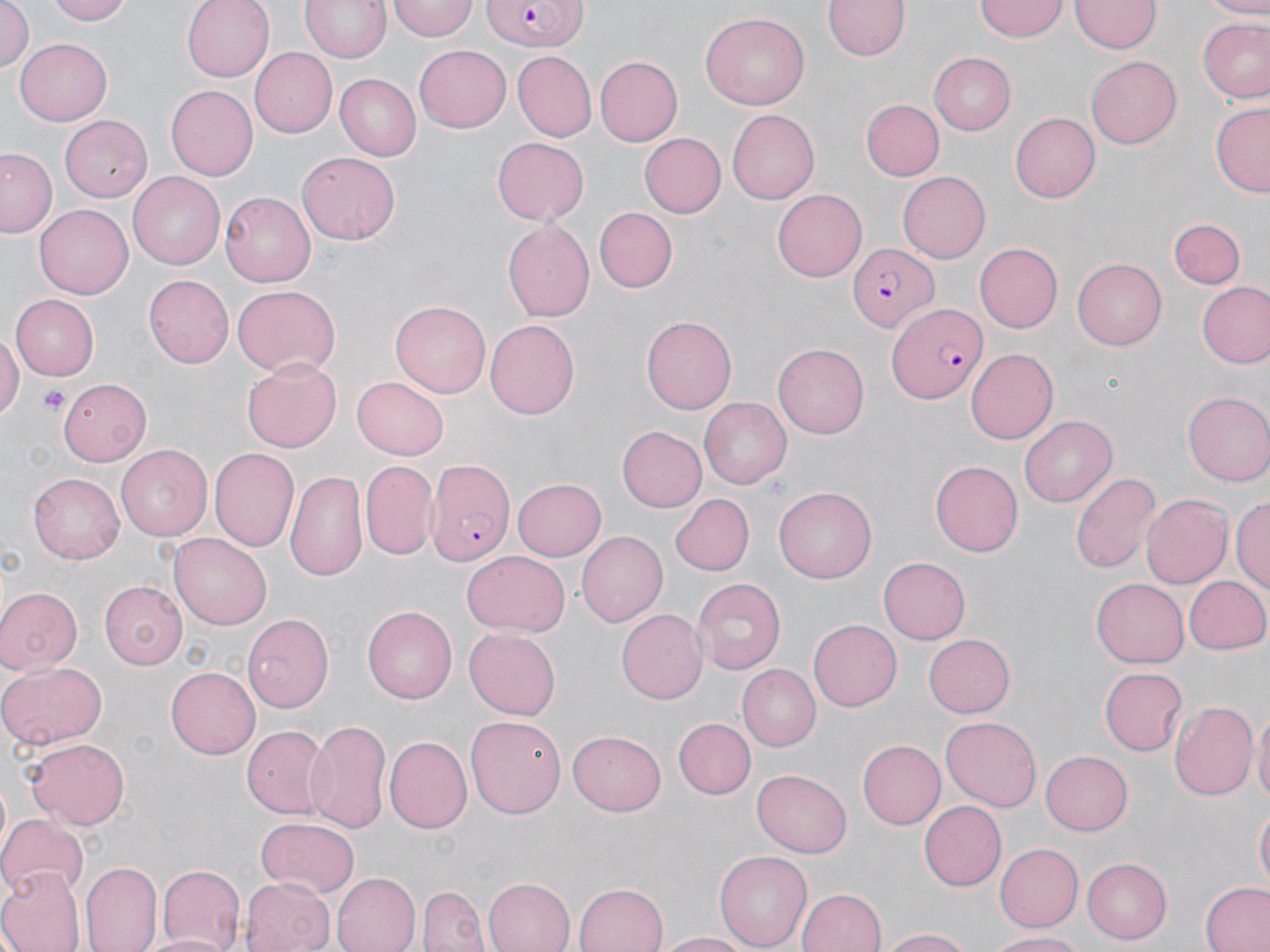
Summary:
  - Coordinate format: approximate bounding boxes as (x1, y1, x2, y2) in pixels
  - Platelet locations: (38, 385, 69, 415)
  - Uninfected red blood cell locations: (43, 0, 137, 25), (181, 0, 275, 82), (299, 0, 391, 64), (388, 0, 477, 41), (825, 0, 908, 62), (975, 0, 1068, 41), (1195, 0, 1270, 16), (1071, 1, 1159, 55), (0, 2, 33, 76), (701, 13, 811, 112), (1197, 18, 1270, 103), (13, 39, 113, 125), (415, 43, 514, 133), (248, 46, 337, 135), (929, 51, 1017, 134), (511, 52, 597, 141), (595, 56, 683, 146), (1087, 56, 1182, 148), (334, 73, 421, 161), (166, 86, 258, 181), (859, 99, 943, 180), (1211, 100, 1270, 197), (725, 109, 818, 204), (1009, 110, 1101, 201), (59, 115, 153, 201), (639, 134, 725, 216), (491, 136, 589, 223), (1, 147, 59, 237), (297, 151, 400, 245), (897, 171, 990, 263), (128, 172, 226, 269), (771, 187, 867, 279), (219, 192, 316, 286), (35, 204, 133, 299), (595, 208, 679, 292), (1169, 217, 1246, 290), (500, 219, 594, 321), (974, 243, 1063, 333), (1072, 257, 1167, 350), (143, 276, 234, 368), (1198, 281, 1270, 369), (230, 285, 341, 378), (10, 295, 100, 379), (391, 298, 490, 396), (641, 315, 737, 414), (485, 319, 580, 420), (0, 332, 21, 426), (772, 343, 869, 438), (965, 350, 1057, 444), (242, 358, 341, 452), (354, 374, 449, 458), (55, 378, 151, 466), (1183, 392, 1270, 488), (699, 399, 792, 490), (1020, 415, 1118, 508), (616, 426, 706, 512), (116, 445, 211, 542), (211, 448, 302, 553), (929, 458, 1022, 554), (361, 459, 437, 559), (284, 467, 369, 584), (1070, 470, 1160, 575), (29, 473, 124, 565), (512, 477, 607, 561), (773, 486, 879, 586), (667, 494, 752, 576), (1142, 494, 1230, 587), (1231, 494, 1270, 593), (577, 530, 667, 626), (168, 534, 272, 630), (462, 550, 569, 635), (879, 556, 970, 644), (691, 576, 784, 674), (1091, 576, 1190, 666), (1182, 576, 1270, 656), (98, 581, 186, 671), (0, 587, 81, 673), (363, 606, 458, 703), (616, 609, 706, 705), (243, 612, 334, 713), (807, 619, 901, 712), (465, 628, 560, 720), (925, 633, 1016, 717), (0, 661, 105, 749), (740, 664, 821, 750), (166, 667, 259, 758), (1100, 668, 1187, 754), (1169, 700, 1256, 803), (1252, 708, 1270, 812), (940, 714, 1043, 811), (467, 715, 568, 818), (307, 718, 391, 832), (673, 718, 755, 799), (243, 723, 327, 818), (567, 730, 667, 816), (25, 736, 130, 829), (385, 736, 472, 834), (856, 739, 945, 830), (1040, 749, 1132, 837), (751, 769, 852, 856), (918, 801, 1005, 890), (1255, 805, 1269, 889), (0, 813, 89, 899), (256, 817, 360, 897), (994, 843, 1082, 933), (714, 849, 811, 950), (1082, 858, 1172, 943), (81, 861, 162, 952), (154, 863, 245, 951), (0, 869, 81, 952), (329, 873, 420, 952), (482, 876, 577, 952), (242, 877, 335, 952), (574, 881, 670, 952), (1201, 881, 1270, 952), (419, 886, 489, 952), (798, 888, 885, 952), (877, 928, 979, 951), (655, 930, 761, 951), (138, 932, 234, 952), (988, 932, 1090, 951)
  - Plasmodium falciparum-infected red blood cell locations: (479, 0, 589, 50), (847, 240, 942, 334), (884, 299, 989, 406), (426, 463, 514, 569)
  - Slide-level diagnosis: Plasmodium falciparum
  - Preparation: thin blood film
  - Stain: May-Grünwald-Giemsa
  - Modality: optical microscopy
  - Image size: 1270×952 pixels
  - Field of view: one of a larger specimen
  - Magnification: 1000x